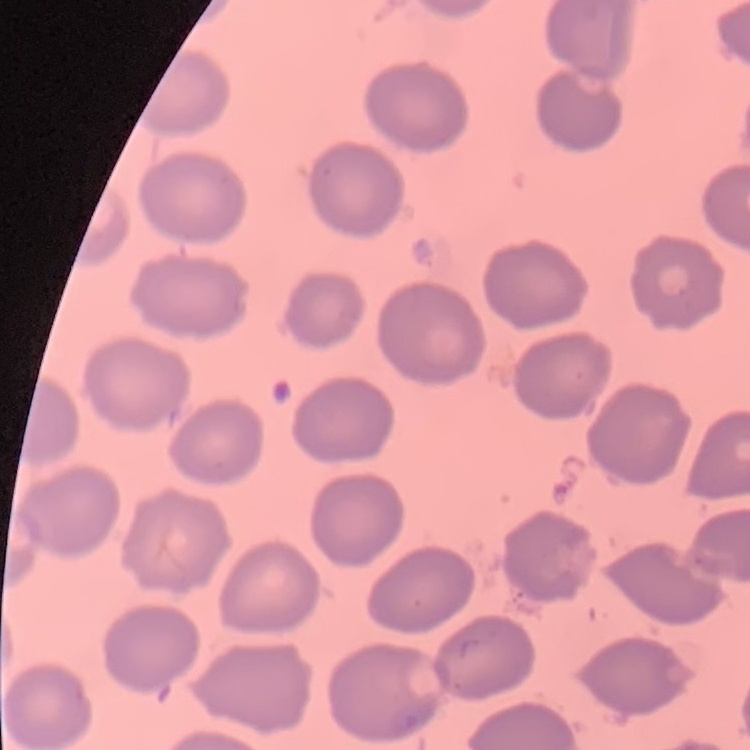
Summary:
  - Erythrocyte morphology: no rouleaux formation
  - Image type: square crop of a larger photomicrograph
  - Stain: Field's or Giemsa
  - Preparation: thin blood smear